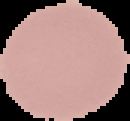

Summary:
  - Malaria status: uninfected
  - Preparation: thin blood film
  - Image type: segmented cell region on a black background
  - Image size: 130×121 pixels